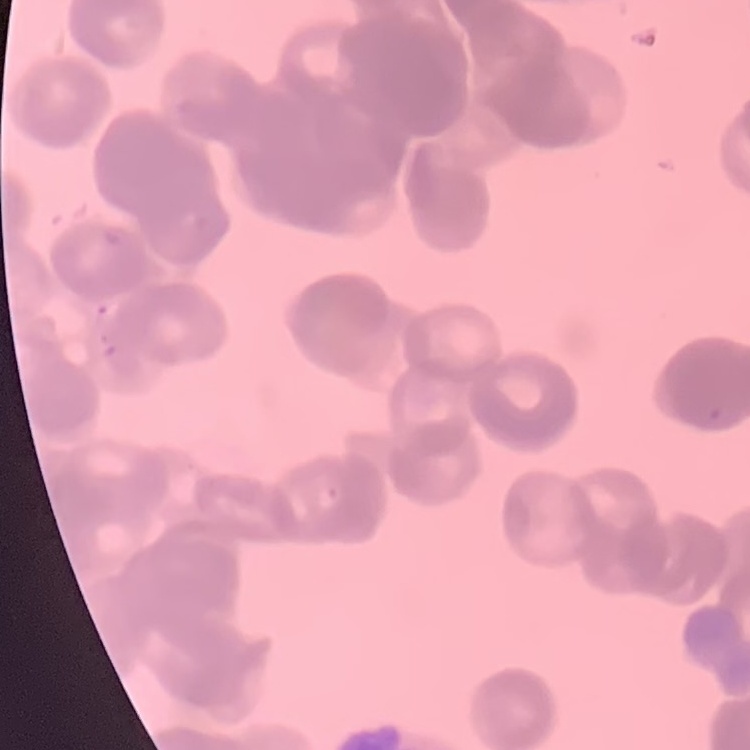 The erythrocytes exhibit rouleaux formation. Thin blood film. Stained with either Field's or Giemsa. Square crop of a larger photomicrograph.